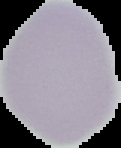
Summary:
  - Preparation: thin blood smear
  - Image type: segmented cell region on a black background
  - Image size: 121×148 pixels
  - Result: negative for malaria parasites